Assess this cell for malaria.
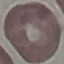
It is uninfected.

image type = automatically extracted cell patch, resized to 64 × 64 pixels
preparation = thin blood smear
stain = Giemsa
capture = smartphone camera at the microscope eyepiece